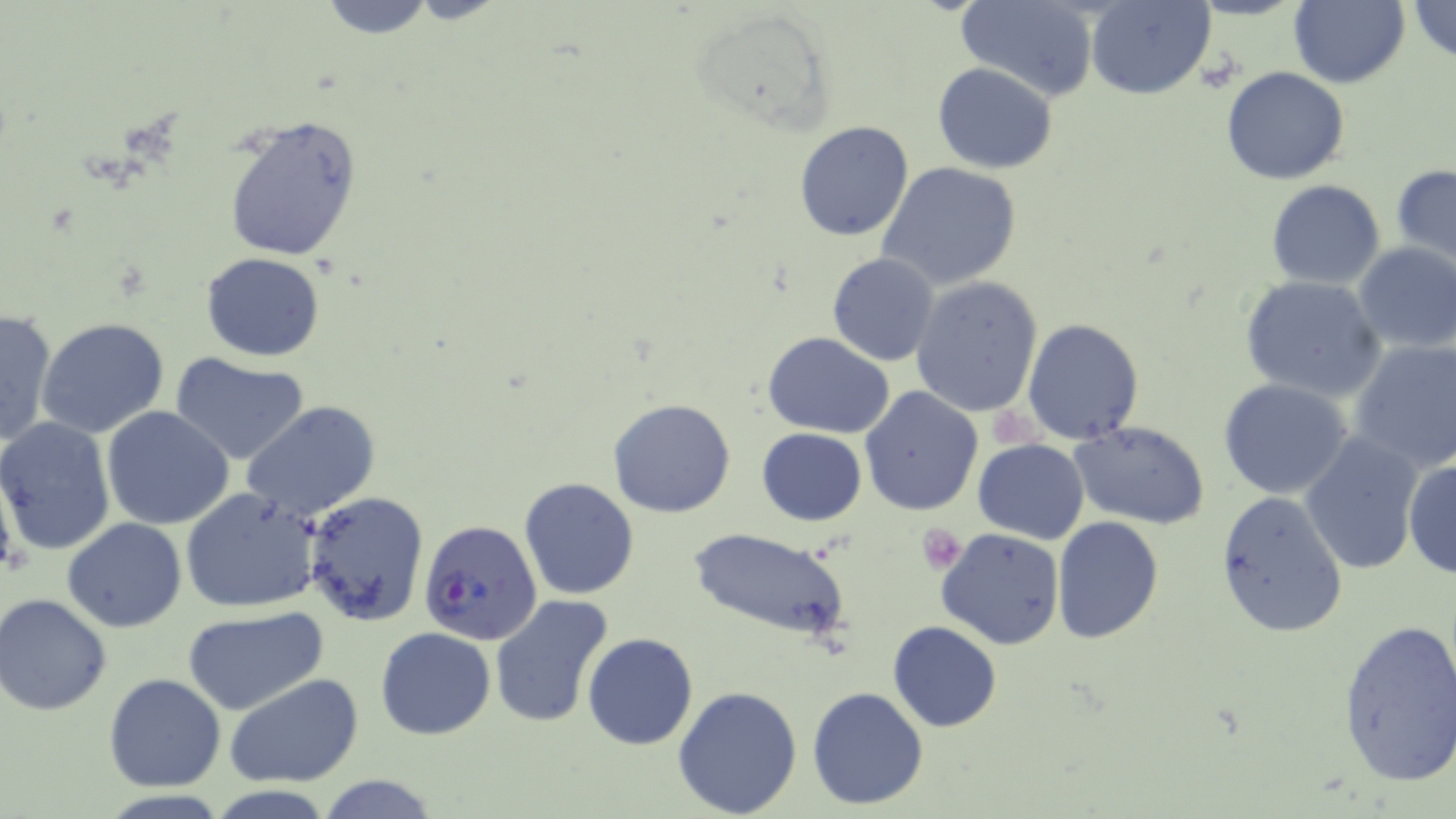
{
  "slide_level_diagnosis": "Plasmodium falciparum",
  "image_size": "1456×819 pixels",
  "plasmodium_falciparum_infected_red_blood_cell_locations": "approximate bounding boxes as (x1,y1)-(x2,y2) corner pairs in pixels: (418,519)-(541,645)",
  "magnification": "1000x",
  "preparation": "thin blood smear",
  "stain": "May-Grünwald-Giemsa",
  "platelet_locations": "approximate bounding boxes as (x1,y1)-(x2,y2) corner pairs in pixels: (988,406)-(1040,450), (919,524)-(966,573)",
  "field_of_view": "one of a larger specimen",
  "modality": "light microscopy",
  "uninfected_red_blood_cell_locations": "approximate bounding boxes as (x1,y1)-(x2,y2) corner pairs in pixels: (316,0)-(439,39), (957,0)-(1101,102), (1086,0)-(1215,99), (1290,0)-(1409,88), (1405,0)-(1456,63), (687,9)-(837,132), (932,63)-(1058,173), (1221,67)-(1349,185), (221,112)-(363,263), (793,121)-(915,242), (876,161)-(1023,291), (1391,162)-(1456,274), (1266,180)-(1385,289), (1353,244)-(1456,354), (200,252)-(326,362), (827,253)-(940,366), (1240,274)-(1386,401), (910,277)-(1043,417), (0,308)-(58,449), (37,317)-(170,440), (1022,318)-(1143,444), (761,331)-(895,439), (1349,339)-(1456,473), (169,351)-(311,464), (1217,378)-(1354,499), (859,387)-(985,517), (608,398)-(737,519), (242,400)-(381,523), (101,406)-(233,531), (0,417)-(116,555), (1069,421)-(1212,529), (757,428)-(866,525), (1300,432)-(1425,573), (973,438)-(1089,543), (0,452)-(24,585), (1402,456)-(1456,580), (517,477)-(640,600), (180,486)-(326,613), (302,490)-(431,628), (1216,491)-(1349,638), (1052,516)-(1164,644), (64,517)-(187,632), (936,527)-(1067,649), (688,528)-(853,644), (1,594)-(115,715), (488,594)-(614,728), (182,605)-(330,715), (1337,615)-(1456,786), (888,621)-(1000,732), (375,627)-(495,740), (583,633)-(698,749), (103,673)-(228,792), (224,673)-(366,789), (672,684)-(803,817), (807,686)-(929,810), (312,775)-(444,817)"
}